Report the malaria status of this cell.
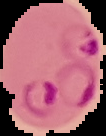
It is parasitized.

Summary:
  - Preparation: thin blood film
  - Image type: segmented cell region with the area outside set to black
  - Image size: 106×136 pixels